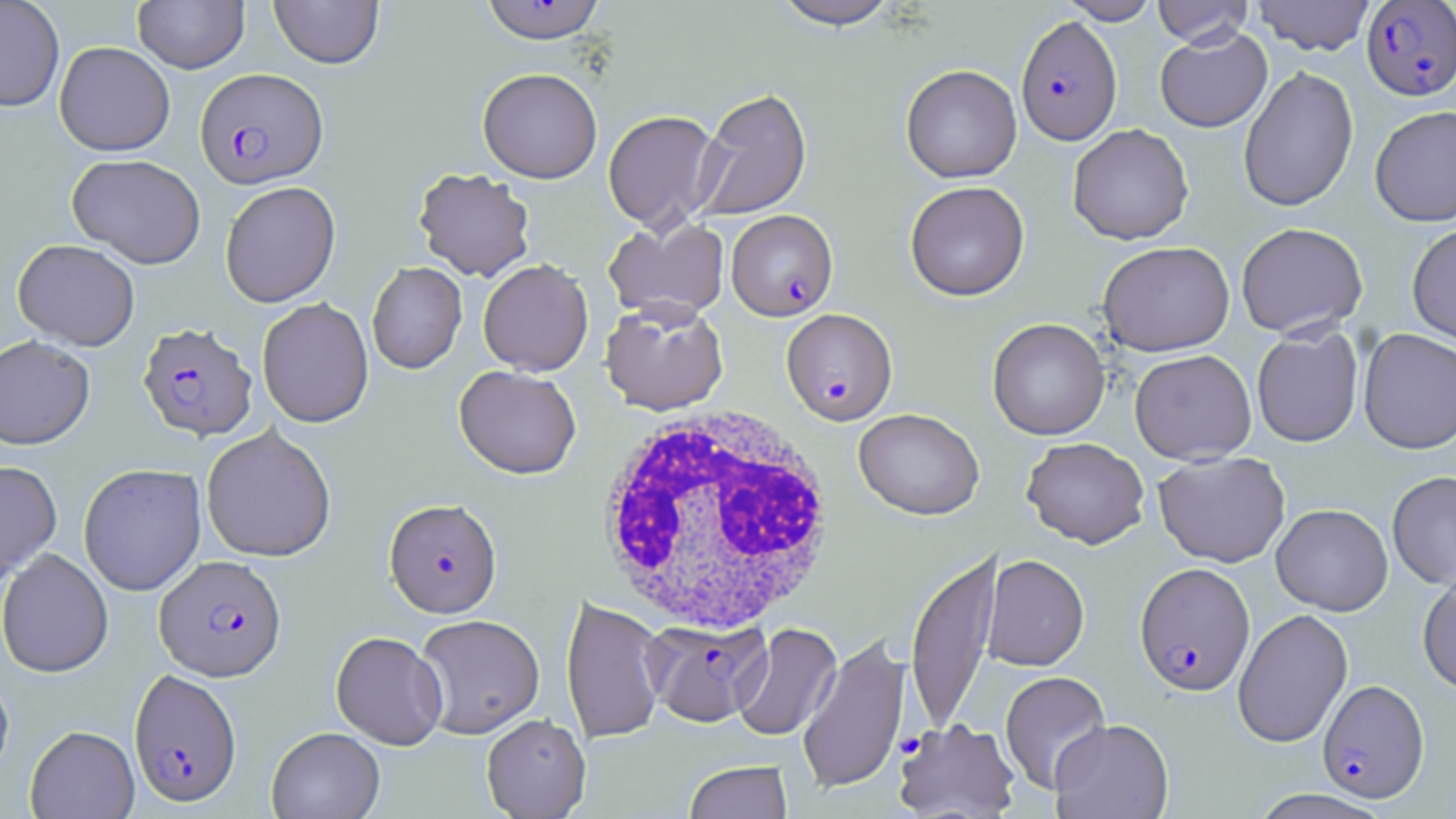
Approximate bounding boxes as (x1,y1)-(x2,y2) corner pairs in pixels. Uninfected red blood cell locations: (0,0)-(65,112), (133,0)-(249,74), (269,0)-(383,69), (769,0)-(903,29), (1057,0)-(1162,24), (1152,0)-(1253,47), (1252,0)-(1375,55), (1155,27)-(1272,132), (54,41)-(175,156), (901,64)-(1022,183), (1238,66)-(1359,212), (477,67)-(602,183), (692,87)-(812,222), (1369,105)-(1456,226), (603,110)-(722,233), (1068,124)-(1194,244), (67,154)-(206,268), (412,167)-(536,282), (220,181)-(341,307), (905,181)-(1030,301), (603,217)-(729,323), (1407,221)-(1456,347), (1235,222)-(1368,338), (13,238)-(140,351), (1097,241)-(1235,356), (478,259)-(594,376), (367,262)-(467,374), (257,297)-(374,427), (600,300)-(729,415), (987,317)-(1110,440), (1251,325)-(1364,447), (1358,329)-(1456,453), (0,335)-(95,449), (1129,349)-(1257,464), (454,365)-(581,479), (853,408)-(985,520), (201,425)-(337,562), (1021,437)-(1150,549), (1153,451)-(1290,567), (0,460)-(62,587), (78,463)-(206,596), (1387,470)-(1456,590), (1271,503)-(1393,615), (0,548)-(113,677), (906,548)-(1002,734), (982,554)-(1089,671), (1417,570)-(1456,696), (561,595)-(667,745), (1233,608)-(1352,747), (414,614)-(545,738), (733,623)-(842,743), (331,631)-(448,749), (798,635)-(910,795), (0,670)-(14,783), (999,671)-(1111,794), (481,713)-(591,819), (1050,718)-(1173,819), (893,719)-(1021,818), (25,725)-(140,819), (266,727)-(384,819), (683,760)-(793,819), (1247,789)-(1393,819). Plasmodium falciparum-infected red blood cell locations: (480,1)-(607,44), (1361,1)-(1456,100), (1016,14)-(1122,145), (195,67)-(328,188), (726,209)-(838,321), (781,308)-(897,425), (137,322)-(258,441), (384,498)-(502,618), (155,554)-(286,681), (1134,562)-(1255,695), (643,619)-(771,727), (129,669)-(242,807), (1317,679)-(1430,803). White blood cell locations: (591,407)-(841,636). Slide-level diagnosis: Plasmodium falciparum. Thin blood film. One field of a larger specimen. Image is 1456×819 pixels. Captured at 1000x magnification. Light microscopy. May-Grünwald-Giemsa-stained preparation.